Locate every blood parasite and identify its species.
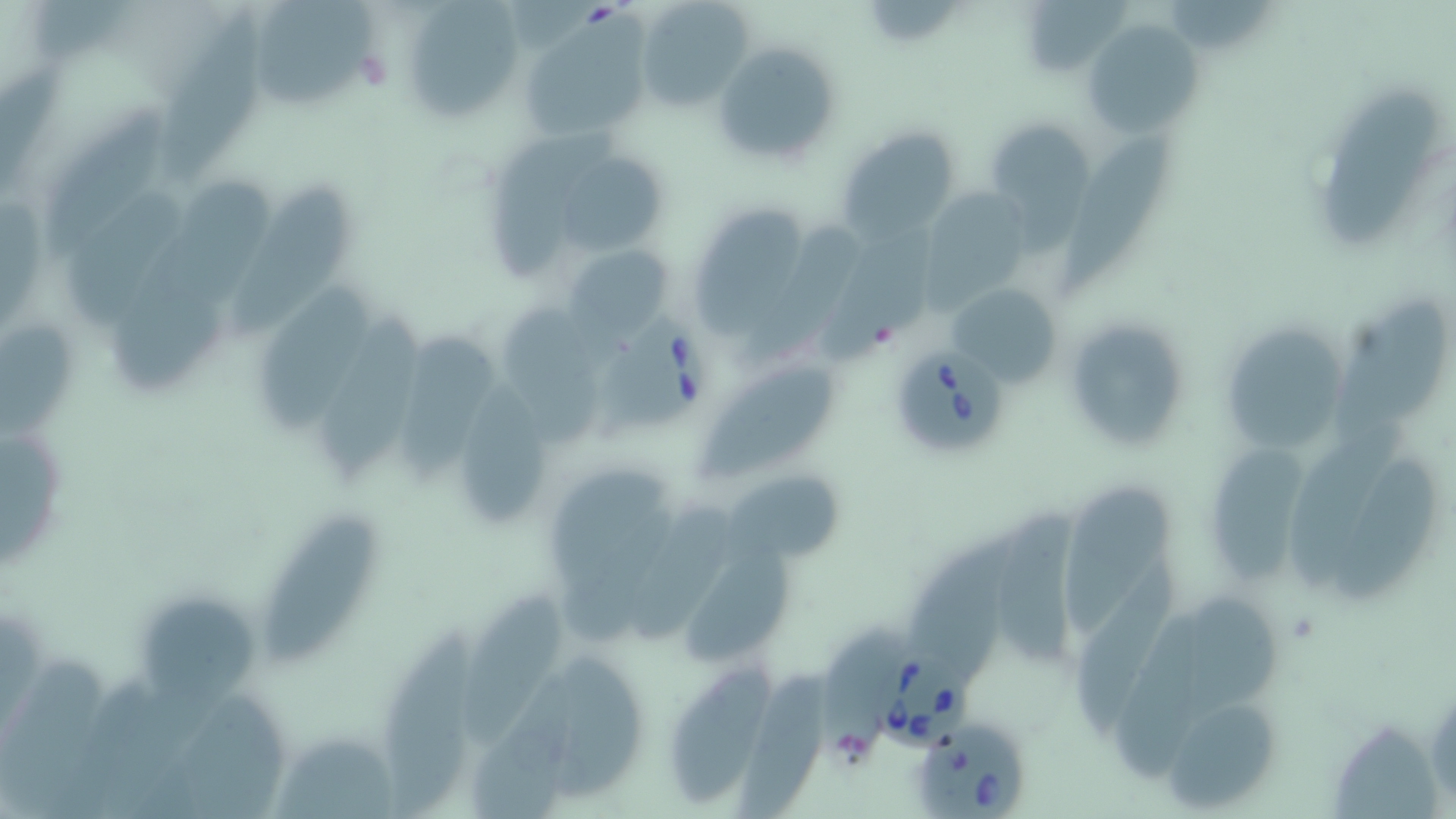

Approximate bounding boxes as named x1/y1/x2/y2 corners in pixels.
Babesia divergens-infected red blood cells: (x1=592, y1=311, x2=714, y2=438), (x1=897, y1=343, x2=1006, y2=455), (x1=868, y1=645, x2=975, y2=749), (x1=918, y1=721, x2=1031, y2=819).
No Plasmodium falciparum, Plasmodium ovale, Plasmodium malariae, Plasmodium vivax, or Trypanosoma brucei observed.

Uninfected red blood cell locations: (x1=255, y1=0, x2=372, y2=106), (x1=635, y1=0, x2=755, y2=112), (x1=1021, y1=1, x2=1135, y2=76), (x1=410, y1=3, x2=523, y2=117), (x1=161, y1=5, x2=269, y2=186), (x1=1085, y1=19, x2=1203, y2=136), (x1=529, y1=22, x2=652, y2=136), (x1=712, y1=40, x2=841, y2=168), (x1=1320, y1=84, x2=1437, y2=249), (x1=47, y1=98, x2=167, y2=261), (x1=985, y1=117, x2=1097, y2=227), (x1=1054, y1=122, x2=1175, y2=298), (x1=840, y1=127, x2=960, y2=240), (x1=489, y1=129, x2=617, y2=285), (x1=565, y1=157, x2=664, y2=253), (x1=64, y1=180, x2=189, y2=332), (x1=234, y1=182, x2=355, y2=336), (x1=918, y1=185, x2=1028, y2=306), (x1=693, y1=204, x2=804, y2=340), (x1=729, y1=220, x2=861, y2=376), (x1=815, y1=227, x2=945, y2=360), (x1=113, y1=238, x2=224, y2=391), (x1=562, y1=242, x2=675, y2=341), (x1=257, y1=277, x2=368, y2=432), (x1=946, y1=282, x2=1062, y2=388), (x1=1331, y1=291, x2=1443, y2=442), (x1=502, y1=298, x2=599, y2=426), (x1=319, y1=312, x2=422, y2=486), (x1=1061, y1=313, x2=1194, y2=449), (x1=401, y1=320, x2=494, y2=486), (x1=0, y1=322, x2=74, y2=443), (x1=1228, y1=325, x2=1342, y2=449), (x1=698, y1=365, x2=839, y2=483), (x1=462, y1=369, x2=543, y2=522), (x1=1282, y1=421, x2=1413, y2=593), (x1=4, y1=424, x2=69, y2=571), (x1=1208, y1=434, x2=1306, y2=588), (x1=1330, y1=455, x2=1439, y2=603), (x1=727, y1=468, x2=845, y2=565), (x1=548, y1=469, x2=671, y2=563), (x1=1063, y1=480, x2=1178, y2=641), (x1=558, y1=503, x2=689, y2=645), (x1=637, y1=503, x2=741, y2=643), (x1=1000, y1=504, x2=1082, y2=668), (x1=259, y1=518, x2=379, y2=666), (x1=914, y1=523, x2=1033, y2=674), (x1=684, y1=541, x2=792, y2=668), (x1=1076, y1=565, x2=1182, y2=732), (x1=469, y1=589, x2=564, y2=744), (x1=138, y1=590, x2=260, y2=714), (x1=1183, y1=593, x2=1287, y2=720), (x1=1112, y1=611, x2=1211, y2=791), (x1=380, y1=623, x2=479, y2=816), (x1=817, y1=632, x2=908, y2=757), (x1=669, y1=661, x2=774, y2=813), (x1=735, y1=665, x2=833, y2=814), (x1=186, y1=686, x2=300, y2=819), (x1=1166, y1=705, x2=1280, y2=809), (x1=274, y1=735, x2=397, y2=819). Platelet locations: (x1=357, y1=45, x2=392, y2=91). Slide-level diagnosis: Babesia divergens. Image is 1456×819 pixels. One field of a larger specimen. May-Grünwald-Giemsa stain. Thin blood film. Captured at 1000x magnification. Optical microscopy.